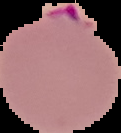

{
  "preparation": "thin blood film",
  "result": "Plasmodium parasites detected",
  "image_type": "cell region segmented out of the field of view; surrounding area masked to black",
  "image_size": "121×133 pixels"
}